Classify this cell by malaria status.
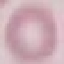

Uninfected.

Summary:
  - Image type: automatically extracted cell patch, resized to 64 × 64 pixels
  - Preparation: thin smear
  - Stain: Giemsa
  - Capture: smartphone through the microscope eyepiece